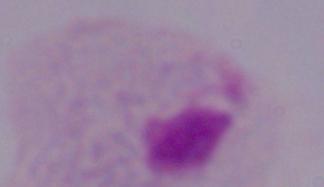
modality: micrograph
identification: trichomonad
magnification: 1000x